Comment on the morphology of the erythrocytes.
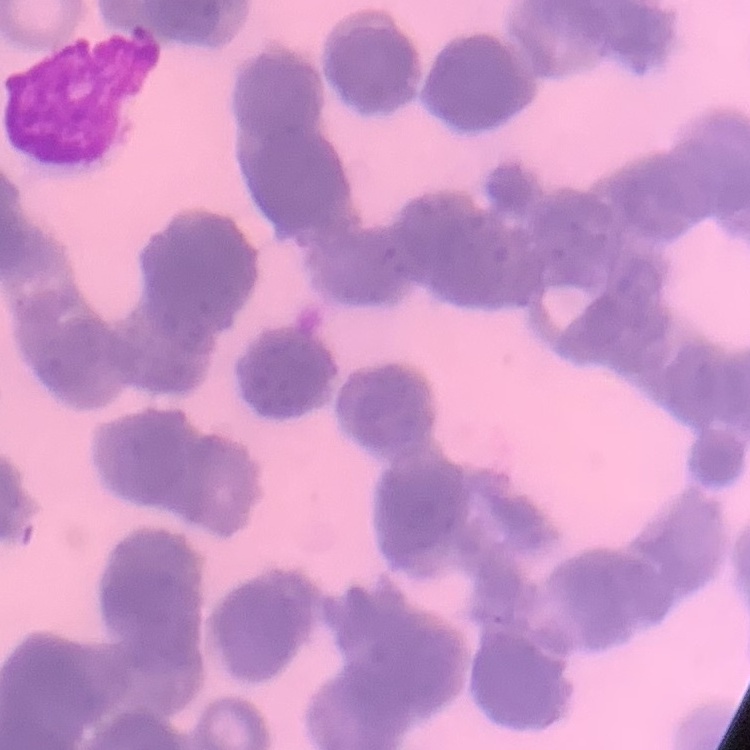
Rouleaux formation.

image type = one tile cut from a larger photomicrograph
stain = Field's or Giemsa
preparation = thin blood smear